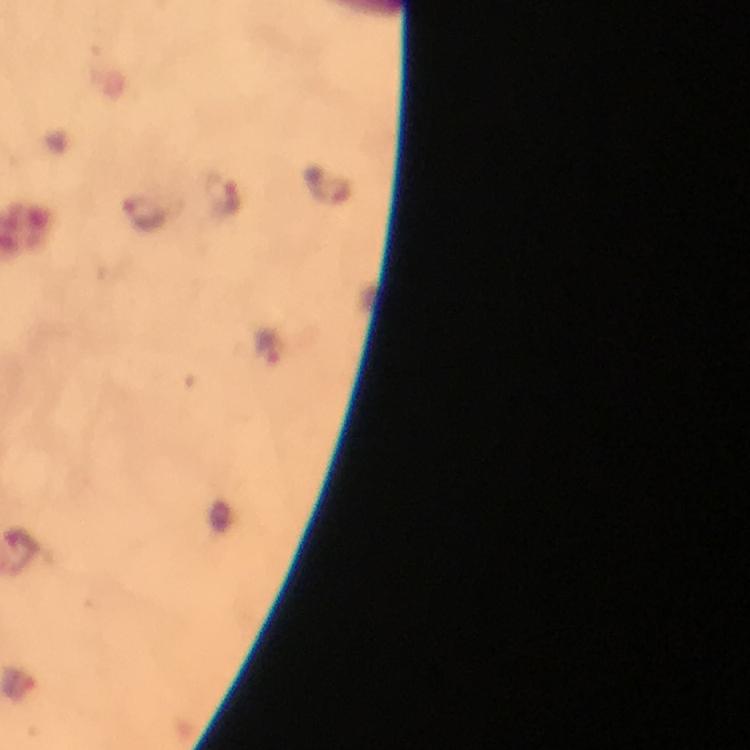

Approximate centers as {x, y} in pixels.
Summary:
  - Malaria parasite locations: {144, 213}
  - Image size: 750×750 pixels
  - Immersion oil: used
  - Cropped from: one field of view
  - Preparation: thick smear
  - Capture: smartphone camera through the microscope
  - Magnification: 100x
  - Context: from a malaria diagnostic workup
  - Stain: Giemsa